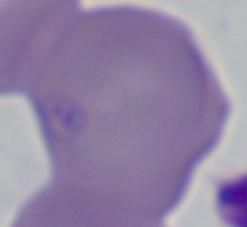
Summary:
  - Identification: Babesia
  - Modality: photomicrograph
  - Magnification: 1000x